Assess this cell for malaria.
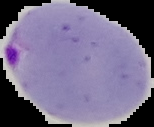
It is parasitized.

{
  "preparation": "thin blood film",
  "image_type": "segmented cell region with the area outside set to black",
  "image_size": "154×127 pixels"
}